Identify the parasite.
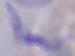

A trypanosome.

modality = photomicrograph
magnification = 1000x